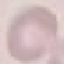
Summary:
  - Result: no malaria parasites seen
  - Preparation: thin blood smear
  - Capture: smartphone through the microscope eyepiece
  - Stain: Giemsa
  - Image type: cell patch, automatically extracted from a larger field of view and resized to 64 × 64 pixels